Outline each blood parasite and name the species.
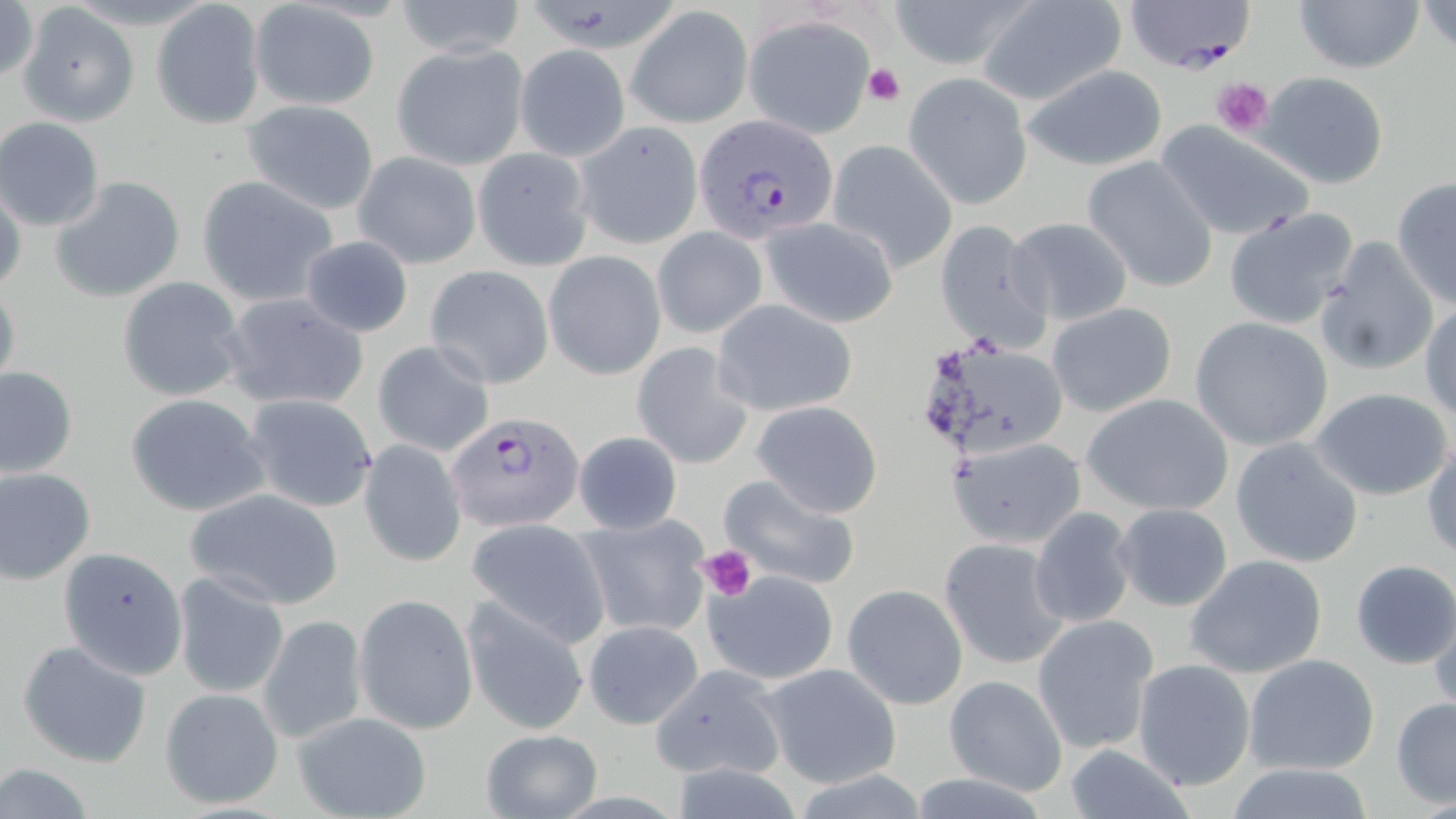
Approximate bounding boxes as named x1/y1/x2/y2 corners in pixels.
Plasmodium falciparum-infected red blood cells: (x1=693, y1=112, x2=839, y2=244), (x1=448, y1=412, x2=584, y2=531).
No Plasmodium ovale, Plasmodium malariae, Plasmodium vivax, Babesia divergens, or Trypanosoma brucei observed.

Uninfected red blood cell locations: (x1=392, y1=0, x2=529, y2=57), (x1=888, y1=0, x2=1029, y2=72), (x1=973, y1=0, x2=1127, y2=107), (x1=1124, y1=0, x2=1255, y2=71), (x1=1294, y1=0, x2=1424, y2=75), (x1=1419, y1=0, x2=1456, y2=52), (x1=150, y1=1, x2=268, y2=128), (x1=0, y1=2, x2=39, y2=86), (x1=247, y1=3, x2=377, y2=112), (x1=626, y1=6, x2=753, y2=127), (x1=21, y1=9, x2=136, y2=125), (x1=744, y1=16, x2=877, y2=139), (x1=390, y1=43, x2=529, y2=170), (x1=513, y1=45, x2=630, y2=161), (x1=1019, y1=63, x2=1169, y2=171), (x1=905, y1=72, x2=1032, y2=208), (x1=1259, y1=72, x2=1389, y2=189), (x1=241, y1=100, x2=379, y2=214), (x1=0, y1=117, x2=105, y2=231), (x1=1156, y1=121, x2=1317, y2=242), (x1=575, y1=126, x2=703, y2=250), (x1=828, y1=140, x2=958, y2=273), (x1=472, y1=147, x2=594, y2=271), (x1=354, y1=152, x2=481, y2=269), (x1=1082, y1=155, x2=1220, y2=294), (x1=50, y1=176, x2=186, y2=304), (x1=195, y1=176, x2=338, y2=307), (x1=1391, y1=177, x2=1455, y2=308), (x1=1, y1=179, x2=26, y2=297), (x1=1223, y1=206, x2=1361, y2=330), (x1=758, y1=216, x2=900, y2=328), (x1=1004, y1=216, x2=1135, y2=325), (x1=934, y1=217, x2=1052, y2=357), (x1=653, y1=227, x2=767, y2=339), (x1=300, y1=237, x2=416, y2=336), (x1=1312, y1=237, x2=1440, y2=374), (x1=544, y1=251, x2=665, y2=380), (x1=424, y1=265, x2=554, y2=388), (x1=0, y1=275, x2=21, y2=396), (x1=116, y1=276, x2=248, y2=401), (x1=219, y1=291, x2=370, y2=413), (x1=713, y1=300, x2=857, y2=418), (x1=1046, y1=302, x2=1177, y2=418), (x1=1420, y1=302, x2=1456, y2=422), (x1=1190, y1=316, x2=1335, y2=454), (x1=913, y1=332, x2=1069, y2=464), (x1=371, y1=340, x2=495, y2=458), (x1=631, y1=342, x2=755, y2=467), (x1=1, y1=365, x2=77, y2=479), (x1=1308, y1=387, x2=1455, y2=501), (x1=125, y1=392, x2=271, y2=517), (x1=1081, y1=393, x2=1234, y2=517), (x1=243, y1=394, x2=380, y2=514), (x1=752, y1=400, x2=883, y2=517), (x1=570, y1=431, x2=684, y2=536), (x1=947, y1=436, x2=1086, y2=549), (x1=1231, y1=438, x2=1364, y2=569), (x1=360, y1=440, x2=467, y2=567), (x1=1424, y1=445, x2=1456, y2=562), (x1=0, y1=467, x2=96, y2=585), (x1=718, y1=473, x2=861, y2=590), (x1=185, y1=486, x2=346, y2=610), (x1=1113, y1=503, x2=1234, y2=612), (x1=1029, y1=507, x2=1136, y2=629), (x1=576, y1=515, x2=713, y2=639), (x1=465, y1=518, x2=611, y2=646), (x1=939, y1=537, x2=1069, y2=670), (x1=53, y1=549, x2=190, y2=696), (x1=1184, y1=554, x2=1329, y2=679), (x1=1350, y1=559, x2=1456, y2=669), (x1=703, y1=569, x2=839, y2=684), (x1=171, y1=571, x2=289, y2=698), (x1=842, y1=584, x2=968, y2=710), (x1=354, y1=593, x2=478, y2=735), (x1=461, y1=596, x2=589, y2=735), (x1=1426, y1=596, x2=1456, y2=716), (x1=257, y1=612, x2=368, y2=746), (x1=1032, y1=615, x2=1159, y2=755), (x1=582, y1=619, x2=704, y2=729), (x1=15, y1=638, x2=154, y2=769), (x1=1244, y1=654, x2=1381, y2=775), (x1=1133, y1=658, x2=1254, y2=791), (x1=758, y1=662, x2=903, y2=788), (x1=648, y1=664, x2=784, y2=783), (x1=944, y1=674, x2=1068, y2=796), (x1=159, y1=687, x2=285, y2=811), (x1=1390, y1=695, x2=1456, y2=809), (x1=289, y1=709, x2=434, y2=819), (x1=477, y1=728, x2=602, y2=818), (x1=1060, y1=745, x2=1201, y2=819), (x1=1218, y1=762, x2=1384, y2=818), (x1=0, y1=763, x2=101, y2=818). Platelet locations: (x1=863, y1=62, x2=906, y2=105), (x1=1210, y1=76, x2=1273, y2=140), (x1=699, y1=545, x2=757, y2=601). Slide-level diagnosis: Plasmodium falciparum. Single field of view. Thin blood film. Captured at 1000x magnification. Image is 1456×819 pixels. May-Grünwald-Giemsa stain. Optical microscopy.